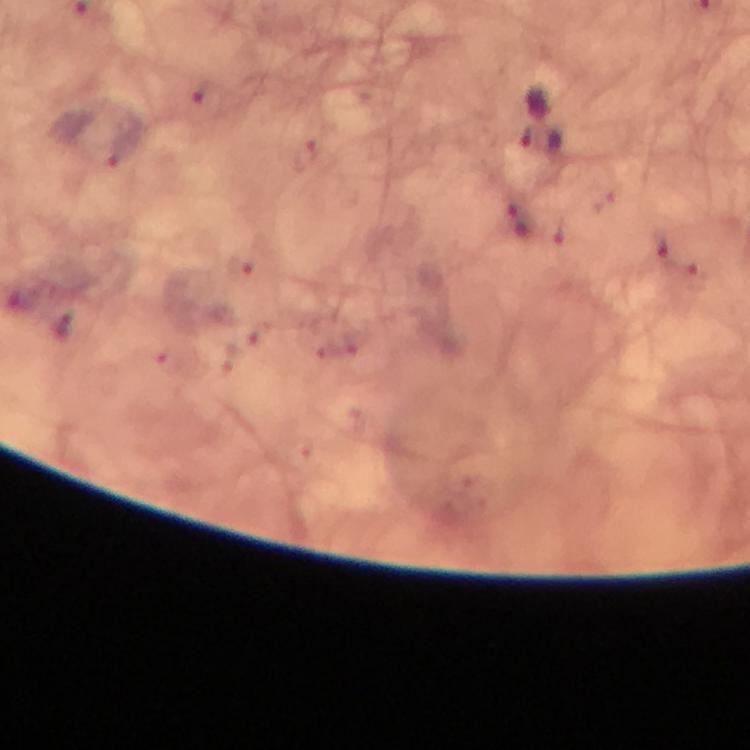

malaria parasite locations = approximate object centers, in pixels from the top-left corner: (x=204, y=93), (x=541, y=141), (x=116, y=154), (x=304, y=156), (x=514, y=204), (x=527, y=231), (x=662, y=249)
context = from a malaria diagnostic workup
magnification = 100x
image size = 750×750 pixels
capture = smartphone photograph through a microscope
preparation = thick blood film
immersion oil = applied
stain = Giemsa
cropped from = one field of view